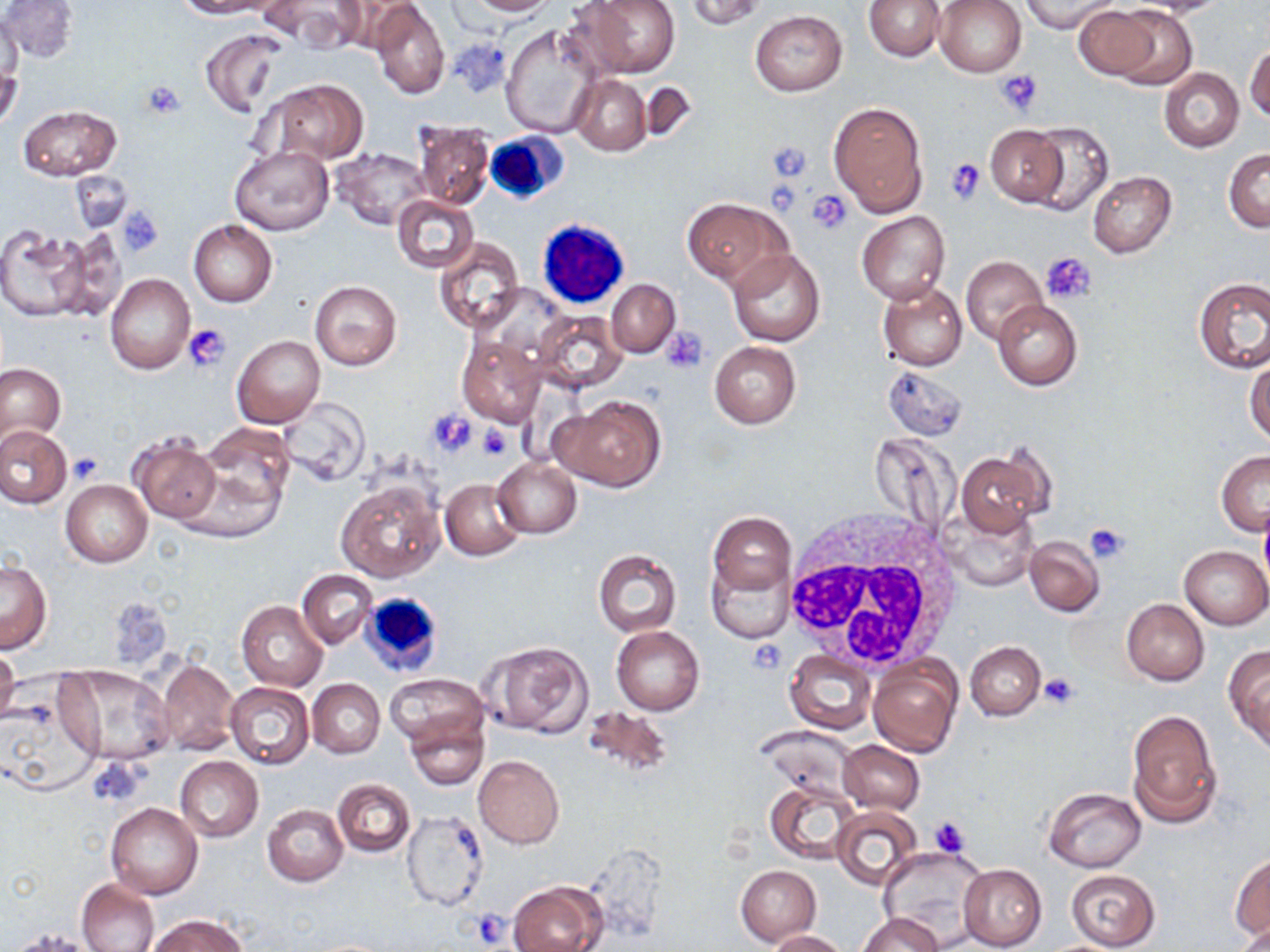
{
  "slide_level_diagnosis": "no evidence of blood parasites",
  "modality": "light microscopy",
  "field_of_view": "one of a larger specimen",
  "stain": "May-Grünwald-Giemsa",
  "magnification": "1000x",
  "platelet_locations": "approximate bounding boxes as (x1,y1)-(x2,y2) corner pairs in pixels: (996,70)-(1042,115), (141,80)-(187,119), (767,143)-(812,183), (945,157)-(986,204), (807,189)-(853,232), (117,208)-(166,257), (1042,252)-(1097,305), (185,323)-(230,371), (663,326)-(709,373), (427,410)-(477,458), (478,422)-(512,461), (68,453)-(103,483), (1085,522)-(1130,563), (746,638)-(785,674), (1040,674)-(1079,710), (91,758)-(142,807), (928,815)-(972,859), (469,908)-(515,943)",
  "uninfected_red_blood_cell_locations": "approximate bounding boxes as (x1,y1)-(x2,y2) corner pairs in pixels: (1,0)-(77,63), (175,0)-(266,17), (464,0)-(557,16), (581,0)-(680,77), (684,0)-(766,29), (865,0)-(944,61), (934,0)-(1026,77), (1018,0)-(1121,32), (1137,0)-(1227,17), (261,1)-(365,50), (332,1)-(422,55), (370,2)-(450,98), (1111,4)-(1196,89), (1073,6)-(1157,79), (749,10)-(847,96), (1,11)-(24,95), (501,23)-(602,139), (200,28)-(287,117), (1246,44)-(1270,123), (0,62)-(23,132), (1159,67)-(1245,152), (569,75)-(652,155), (264,80)-(368,165), (639,82)-(698,141), (829,102)-(927,216), (17,105)-(120,180), (1026,120)-(1113,217), (413,121)-(495,208), (985,124)-(1067,206), (229,146)-(333,236), (332,148)-(434,229), (1223,148)-(1270,232), (70,171)-(132,232), (1088,171)-(1175,258), (392,194)-(479,273), (682,197)-(788,288), (857,211)-(950,303), (188,220)-(277,306), (1,227)-(93,322), (51,229)-(130,322), (434,238)-(524,332), (726,247)-(825,347), (961,256)-(1048,345), (105,273)-(195,374), (1193,277)-(1270,372), (309,279)-(401,370), (607,279)-(680,357), (878,282)-(967,371), (992,299)-(1082,390), (534,311)-(627,393), (457,332)-(546,427), (233,335)-(325,430), (710,342)-(801,428), (1246,355)-(1270,446), (0,364)-(65,445), (883,365)-(967,440), (556,394)-(666,492), (278,399)-(369,486), (200,423)-(294,513), (0,424)-(71,508), (129,434)-(221,523), (958,450)-(1046,535), (1216,451)-(1270,536), (492,456)-(581,538), (439,478)-(527,562), (61,479)-(152,567), (336,479)-(444,582), (943,503)-(1037,593), (707,511)-(794,596), (1024,535)-(1104,616), (1180,545)-(1270,629), (594,549)-(681,637), (707,559)-(791,642), (1,560)-(51,652), (298,568)-(378,649), (1121,599)-(1209,685), (237,600)-(327,691), (612,626)-(704,716), (482,641)-(595,737), (966,641)-(1046,721), (1224,645)-(1270,751), (785,648)-(876,733), (0,654)-(19,719), (867,654)-(961,758), (155,658)-(240,757), (58,666)-(174,766), (385,674)-(487,750), (308,679)-(385,758), (226,682)-(315,769), (2,688)-(102,799), (579,706)-(675,782), (1126,708)-(1221,828), (405,713)-(489,790), (838,740)-(924,815), (473,753)-(565,848), (175,756)-(262,841), (333,779)-(416,857), (766,781)-(860,863), (1042,787)-(1146,871), (262,803)-(347,886), (106,804)-(202,900), (834,807)-(922,891), (400,810)-(489,912), (880,846)-(989,947), (1231,854)-(1270,940), (958,864)-(1047,949), (735,865)-(822,945), (1065,869)-(1160,949), (75,877)-(159,952), (508,881)-(606,952), (859,912)-(941,951), (146,914)-(250,952), (1235,922)-(1268,952), (8,928)-(102,952), (765,929)-(848,951)",
  "white_blood_cell_locations": "approximate bounding boxes as (x1,y1)-(x2,y2) corner pairs in pixels: (483,131)-(568,204), (539,218)-(629,309), (782,508)-(969,675), (357,591)-(445,677)",
  "image_size": "1270×952 pixels",
  "preparation": "thin blood film"
}